Identify the parasite.
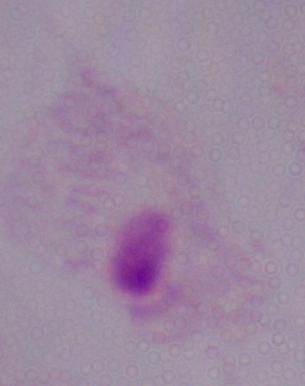
This is a trichomonad.

Summary:
  - Modality: micrograph
  - Magnification: 1000x